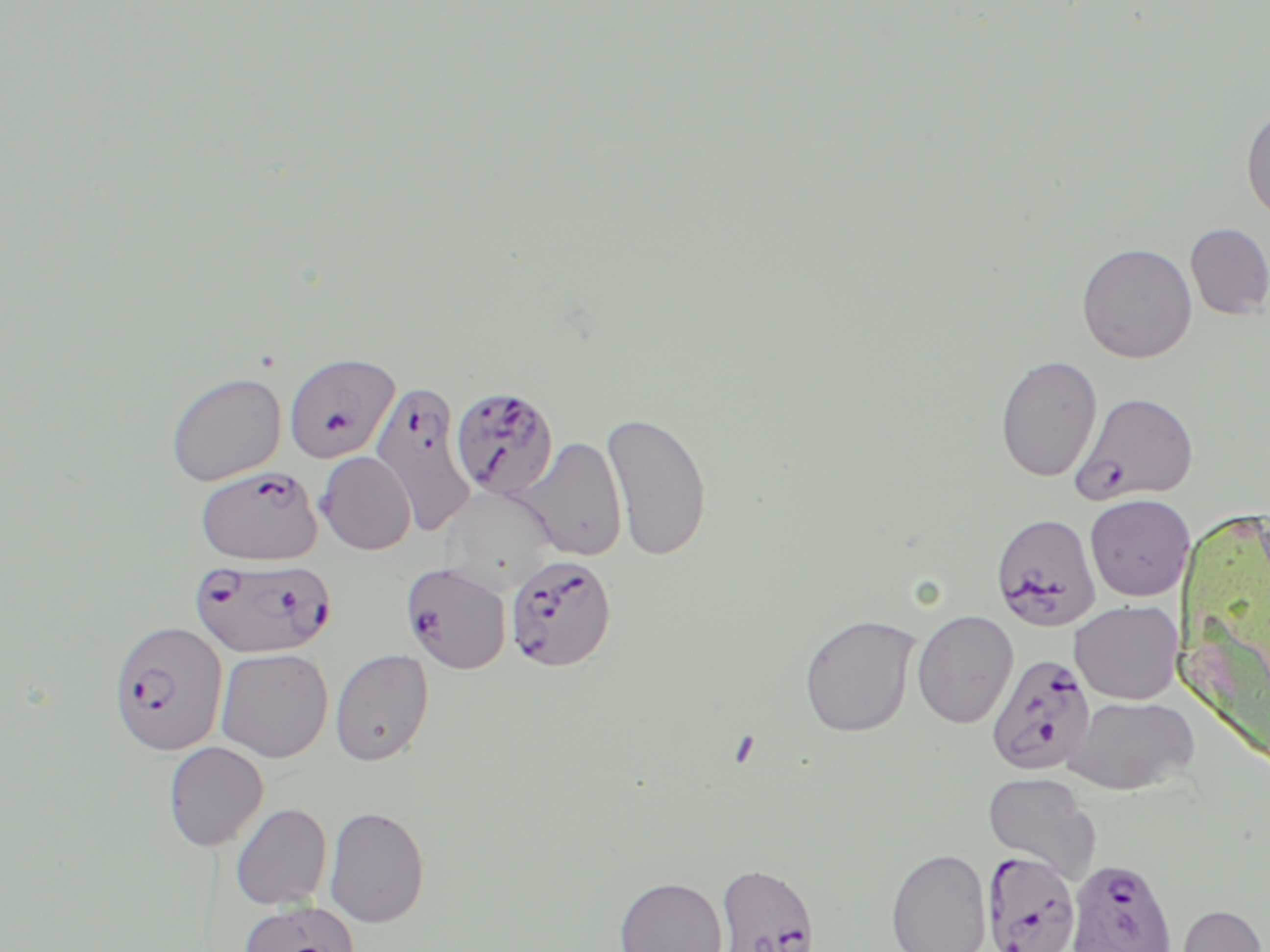 Approximate bounding boxes as [x1, y1, x2, y2] in pixels. Plasmodium falciparum-infected red blood cell locations: [283, 352, 400, 463], [369, 380, 478, 534], [450, 385, 559, 498], [1069, 391, 1200, 505], [194, 465, 322, 565], [990, 513, 1102, 632], [505, 553, 617, 673], [191, 556, 337, 658], [400, 563, 511, 674], [116, 622, 226, 754], [985, 653, 1095, 776], [980, 851, 1082, 952], [1065, 857, 1178, 952], [713, 862, 821, 952]. Uninfected red blood cell locations: [1241, 103, 1270, 226], [1184, 223, 1270, 320], [1076, 241, 1197, 363], [994, 353, 1103, 483], [165, 372, 286, 486], [602, 410, 713, 562], [518, 436, 627, 561], [315, 451, 417, 555], [1084, 494, 1194, 601], [1069, 600, 1183, 704], [912, 610, 1019, 729], [798, 614, 920, 737], [215, 647, 333, 763], [330, 648, 435, 766], [1063, 695, 1198, 795], [162, 741, 269, 851], [982, 772, 1101, 881], [231, 803, 332, 910], [324, 805, 430, 928], [885, 847, 992, 952], [614, 875, 728, 952], [237, 900, 361, 952], [1175, 903, 1267, 952]. Slide-level diagnosis: Plasmodium falciparum. Single field of view. May-Grünwald-Giemsa-stained preparation. Optical microscopy. Thin blood film. Captured at 1000x magnification. Image is 1270×952 pixels.